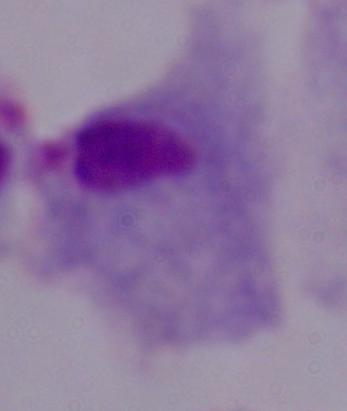
Summary:
  - Magnification: 1000x
  - Identification: trichomonad
  - Modality: photomicrograph